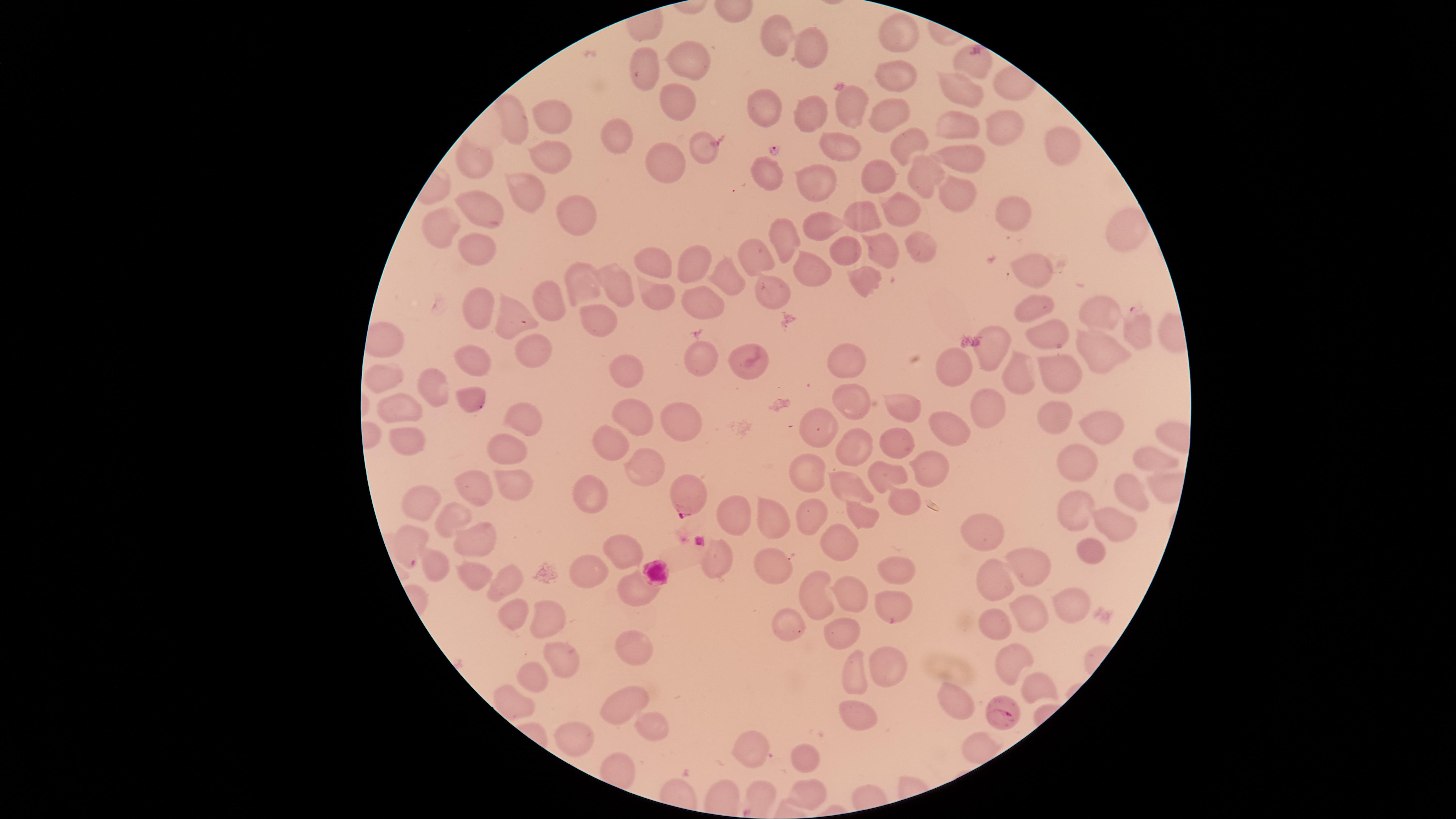

visible region = circular
preparation = thin smear of blood
uninfected red blood cells = approximate marker points as (x, y) in pixels: (773, 31), (896, 37), (815, 45), (688, 58), (646, 65), (974, 65), (901, 76), (963, 89), (678, 97), (757, 107), (851, 108), (806, 110), (550, 114), (888, 115), (957, 119), (510, 121), (994, 125), (611, 133), (904, 139), (840, 143), (1059, 144), (697, 153), (661, 156), (544, 157), (963, 157), (472, 167), (763, 173), (879, 177), (919, 178), (818, 182), (522, 190), (955, 194), (906, 206), (1020, 213), (481, 215), (865, 219), (576, 220), (440, 227), (824, 228), (1125, 231), (784, 240), (477, 243), (922, 245), (878, 248), (755, 255), (843, 255), (696, 264), (655, 267), (1036, 273), (808, 276), (722, 277), (865, 279), (577, 281), (620, 281), (769, 293), (660, 295), (702, 298), (548, 302), (1025, 308), (1103, 311), (477, 312), (511, 319), (597, 325), (1039, 336), (991, 347), (1103, 348), (529, 353), (479, 360), (702, 361), (741, 363), (854, 364), (953, 364), (629, 368), (388, 374), (1022, 375), (1058, 376), (439, 382), (851, 398), (469, 400), (897, 400), (397, 405), (982, 405), (1046, 412), (523, 417), (632, 418), (682, 420), (823, 424), (1093, 424), (946, 428), (900, 436), (411, 439), (853, 439), (511, 444), (608, 444), (1078, 458), (1145, 461), (644, 467), (928, 468), (809, 471), (887, 473), (511, 483), (471, 485), (847, 488), (1123, 488), (589, 489), (900, 500), (425, 505), (810, 507), (1071, 510), (731, 514), (451, 519), (860, 519), (773, 526), (1115, 526), (986, 529), (833, 542), (1087, 548), (624, 550), (469, 551), (712, 560), (436, 561), (1030, 561), (772, 562), (895, 570), (586, 573), (467, 574), (996, 578), (508, 581), (633, 588), (821, 589), (853, 592), (1070, 596), (890, 605), (508, 614), (994, 615), (1024, 617), (539, 620), (787, 622), (841, 632), (633, 651), (553, 656), (1006, 660), (888, 666), (851, 670), (524, 680), (1045, 688), (958, 698), (623, 701), (852, 715), (646, 722), (579, 731), (754, 749), (804, 759), (806, 792)
field of view = single
presence = malaria parasites identified
species = Plasmodium falciparum
image size = 1456×819 pixels
stain = Giemsa
parasitized red blood cells = approximate marker points as (x, y) in pixels: (1138, 330), (688, 500), (410, 543), (1013, 716)
capture = smartphone photograph through the microscope eyepiece